State which cell type is depicted.
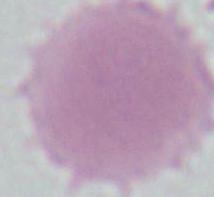
An erythrocyte.

Summary:
  - Magnification: 1000x
  - Modality: photomicrograph